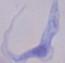

A trypanosome is shown. 1000x magnification. Photomicrograph.